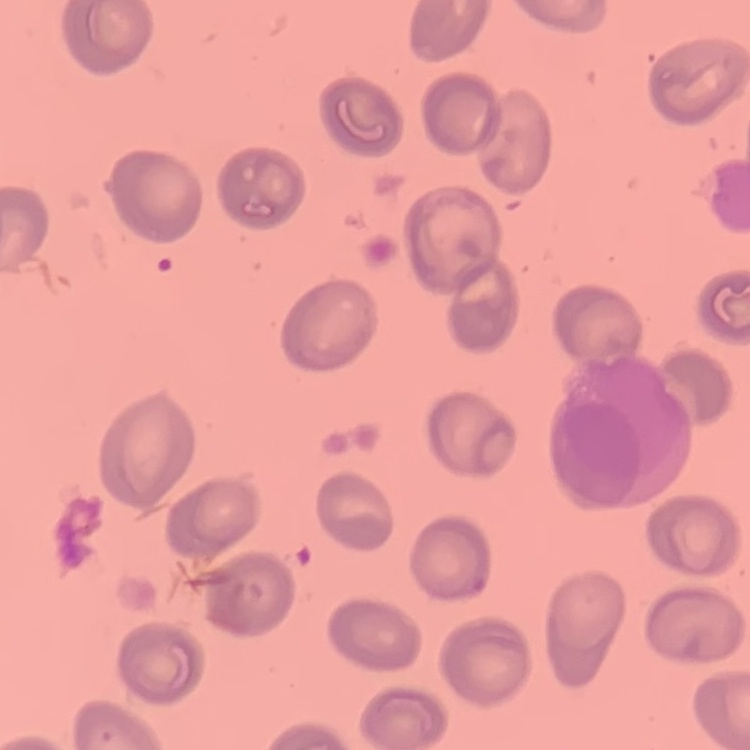 The erythrocytes show no rouleaux formation. Thin blood film. Square crop of a larger photomicrograph. Stained with either Field's or Giemsa.